Outline each blood parasite and name the species.
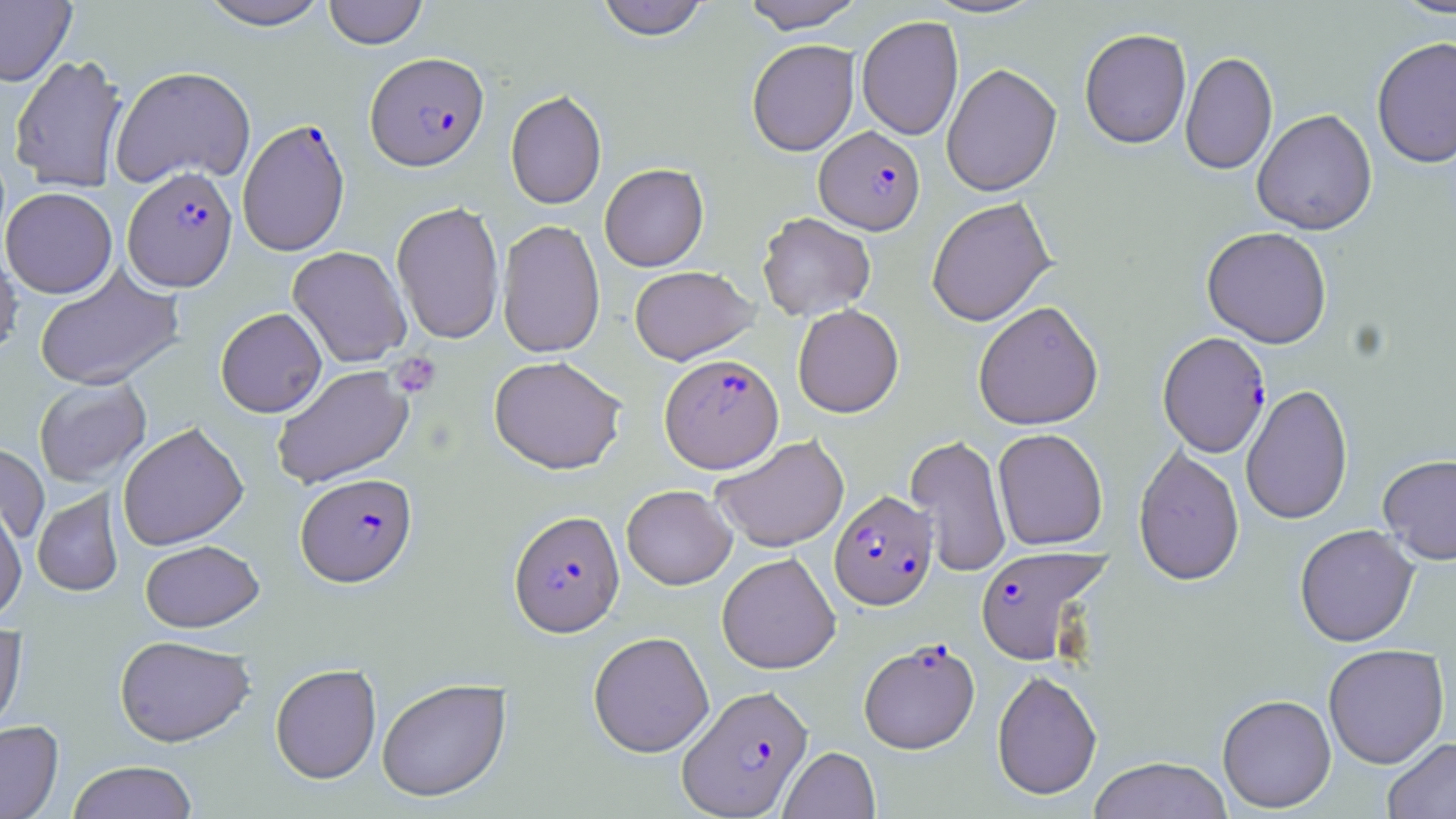
Approximate bounding boxes as named x1/y1/x2/y2 corners in pixels.
Plasmodium falciparum-infected red blood cells: (x1=365, y1=52, x2=489, y2=170), (x1=237, y1=117, x2=351, y2=256), (x1=814, y1=125, x2=924, y2=235), (x1=122, y1=167, x2=238, y2=291), (x1=1156, y1=332, x2=1271, y2=457), (x1=660, y1=354, x2=784, y2=473), (x1=296, y1=472, x2=417, y2=586), (x1=830, y1=490, x2=937, y2=610), (x1=509, y1=509, x2=624, y2=636), (x1=976, y1=544, x2=1110, y2=665), (x1=859, y1=639, x2=980, y2=753), (x1=677, y1=684, x2=813, y2=818).
No Plasmodium ovale, Plasmodium malariae, Plasmodium vivax, Babesia divergens, or Trypanosoma brucei observed.

Platelet locations: (x1=389, y1=351, x2=442, y2=398). Uninfected red blood cell locations: (x1=0, y1=0, x2=76, y2=86), (x1=196, y1=0, x2=331, y2=30), (x1=322, y1=0, x2=428, y2=48), (x1=594, y1=0, x2=711, y2=41), (x1=742, y1=0, x2=864, y2=33), (x1=924, y1=0, x2=1048, y2=19), (x1=1391, y1=0, x2=1456, y2=20), (x1=857, y1=16, x2=964, y2=140), (x1=1079, y1=28, x2=1192, y2=148), (x1=1371, y1=36, x2=1456, y2=169), (x1=747, y1=39, x2=860, y2=156), (x1=1180, y1=50, x2=1277, y2=175), (x1=9, y1=54, x2=128, y2=193), (x1=941, y1=63, x2=1062, y2=196), (x1=110, y1=66, x2=256, y2=189), (x1=505, y1=89, x2=607, y2=209), (x1=1252, y1=109, x2=1377, y2=235), (x1=599, y1=163, x2=708, y2=271), (x1=1, y1=187, x2=117, y2=298), (x1=927, y1=197, x2=1056, y2=326), (x1=391, y1=201, x2=505, y2=344), (x1=757, y1=212, x2=875, y2=320), (x1=497, y1=219, x2=605, y2=358), (x1=1202, y1=226, x2=1332, y2=348), (x1=0, y1=244, x2=22, y2=362), (x1=288, y1=246, x2=411, y2=367), (x1=33, y1=265, x2=185, y2=391), (x1=629, y1=265, x2=758, y2=365), (x1=973, y1=300, x2=1104, y2=430), (x1=792, y1=304, x2=904, y2=417), (x1=215, y1=307, x2=326, y2=418), (x1=489, y1=355, x2=627, y2=474), (x1=271, y1=365, x2=414, y2=489), (x1=34, y1=377, x2=151, y2=487), (x1=1241, y1=383, x2=1353, y2=525), (x1=118, y1=422, x2=249, y2=551), (x1=993, y1=428, x2=1107, y2=550), (x1=905, y1=433, x2=1011, y2=578), (x1=711, y1=434, x2=849, y2=552), (x1=0, y1=441, x2=49, y2=545), (x1=1133, y1=444, x2=1244, y2=586), (x1=1377, y1=453, x2=1456, y2=565), (x1=622, y1=484, x2=737, y2=589), (x1=32, y1=489, x2=124, y2=597), (x1=0, y1=499, x2=27, y2=622), (x1=1294, y1=524, x2=1419, y2=647), (x1=140, y1=540, x2=264, y2=632), (x1=716, y1=553, x2=841, y2=674), (x1=0, y1=626, x2=27, y2=746), (x1=588, y1=631, x2=714, y2=757), (x1=115, y1=634, x2=254, y2=747), (x1=1323, y1=643, x2=1449, y2=768), (x1=270, y1=663, x2=382, y2=783), (x1=991, y1=669, x2=1102, y2=800), (x1=376, y1=677, x2=512, y2=802), (x1=1217, y1=694, x2=1337, y2=813), (x1=0, y1=719, x2=63, y2=818), (x1=1382, y1=737, x2=1456, y2=819), (x1=779, y1=746, x2=880, y2=818), (x1=1088, y1=756, x2=1232, y2=819), (x1=66, y1=760, x2=199, y2=819). Slide-level diagnosis: Plasmodium falciparum. May-Grünwald-Giemsa stain. One field of a larger specimen. Image is 1456×819 pixels. Light microscopy. Thin blood film. 1000x magnification.